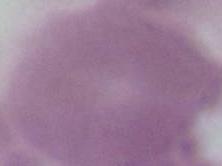 1000x magnification. An erythrocyte is seen. Micrograph.